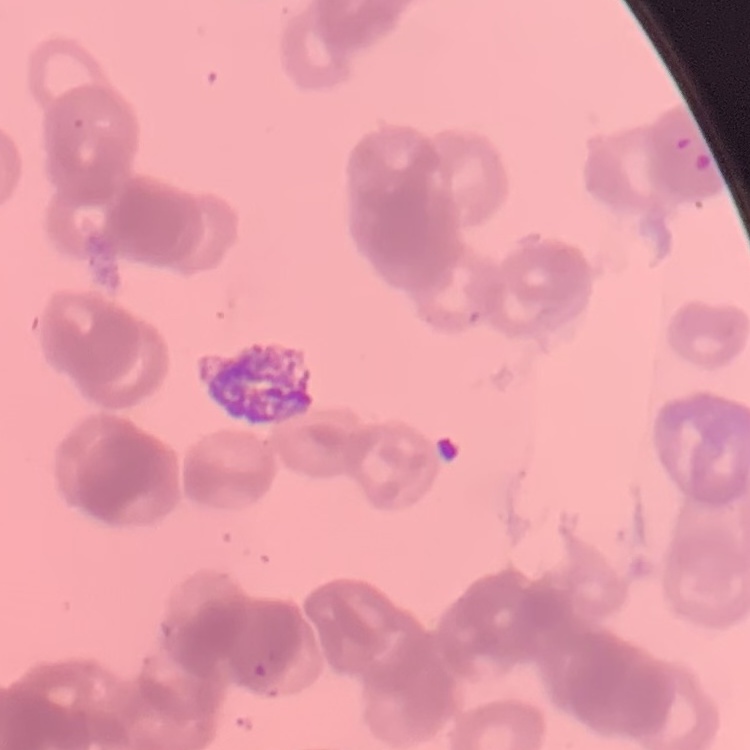
Summary:
  - Erythrocyte morphology: rouleaux formation
  - Image type: one tile cut from a larger photomicrograph
  - Stain: Field's or Giemsa
  - Preparation: thin blood film